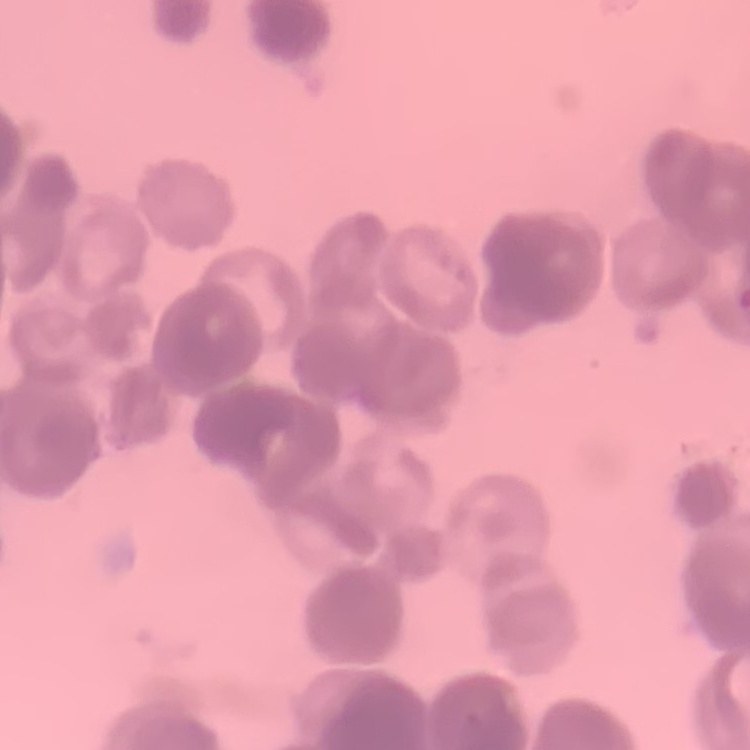
The red blood cells show rouleaux formation. Thin blood film. Stained with either Field's or Giemsa. Square crop of a larger photomicrograph.